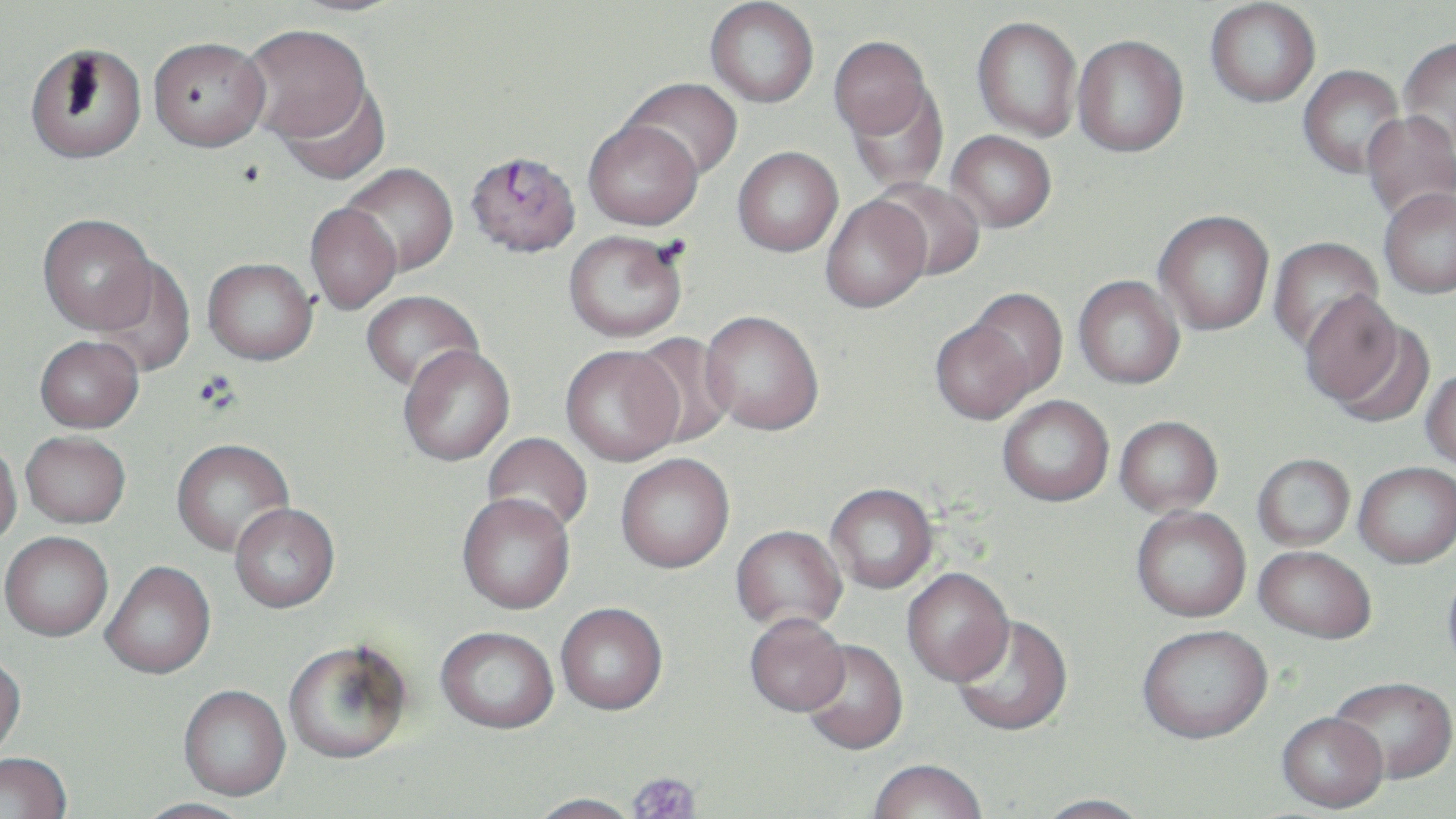
slide_level_diagnosis: Plasmodium falciparum
image_size: 1456×819 pixels
preparation: thin blood film
uninfected_red_blood_cell_locations: 'approximate bounding boxes as named x1/y1/x2/y2 corners in pixels: (x1=285, y1=0, x2=411, y2=17), (x1=705, y1=1, x2=819, y2=107), (x1=1205, y1=1, x2=1321, y2=107), (x1=972, y1=16, x2=1083, y2=141), (x1=241, y1=24, x2=373, y2=144), (x1=1072, y1=35, x2=1189, y2=157), (x1=148, y1=36, x2=270, y2=151), (x1=829, y1=36, x2=933, y2=139), (x1=1398, y1=36, x2=1456, y2=156), (x1=24, y1=42, x2=148, y2=165), (x1=1298, y1=65, x2=1405, y2=178), (x1=621, y1=77, x2=743, y2=182), (x1=275, y1=79, x2=391, y2=185), (x1=844, y1=83, x2=948, y2=191), (x1=1360, y1=111, x2=1456, y2=224), (x1=583, y1=119, x2=703, y2=230), (x1=946, y1=130, x2=1056, y2=232), (x1=733, y1=146, x2=843, y2=256), (x1=340, y1=163, x2=459, y2=276), (x1=872, y1=178, x2=986, y2=280), (x1=1379, y1=187, x2=1456, y2=298), (x1=820, y1=195, x2=930, y2=313), (x1=304, y1=203, x2=402, y2=314), (x1=1153, y1=210, x2=1274, y2=335), (x1=37, y1=213, x2=157, y2=334), (x1=563, y1=230, x2=687, y2=342), (x1=1267, y1=237, x2=1385, y2=357), (x1=92, y1=256, x2=198, y2=377), (x1=202, y1=257, x2=318, y2=364), (x1=1073, y1=275, x2=1185, y2=389), (x1=964, y1=287, x2=1068, y2=399), (x1=360, y1=290, x2=483, y2=393), (x1=1299, y1=290, x2=1407, y2=411), (x1=700, y1=310, x2=823, y2=434), (x1=930, y1=317, x2=1036, y2=425), (x1=629, y1=332, x2=738, y2=449), (x1=35, y1=335, x2=143, y2=433), (x1=398, y1=345, x2=515, y2=466), (x1=560, y1=345, x2=683, y2=465), (x1=1421, y1=368, x2=1456, y2=471), (x1=997, y1=395, x2=1114, y2=507), (x1=1114, y1=416, x2=1223, y2=517), (x1=21, y1=433, x2=130, y2=531), (x1=482, y1=433, x2=593, y2=536), (x1=171, y1=438, x2=294, y2=557), (x1=0, y1=441, x2=23, y2=550), (x1=616, y1=454, x2=735, y2=573), (x1=1252, y1=454, x2=1355, y2=551), (x1=1354, y1=462, x2=1456, y2=568), (x1=825, y1=484, x2=937, y2=594), (x1=456, y1=496, x2=575, y2=616), (x1=230, y1=505, x2=339, y2=615), (x1=1131, y1=506, x2=1251, y2=623), (x1=731, y1=526, x2=847, y2=635), (x1=0, y1=535, x2=113, y2=644), (x1=1253, y1=545, x2=1377, y2=644), (x1=101, y1=564, x2=216, y2=682), (x1=1443, y1=564, x2=1456, y2=682), (x1=901, y1=569, x2=1015, y2=688), (x1=555, y1=606, x2=668, y2=718), (x1=950, y1=616, x2=1072, y2=739), (x1=744, y1=617, x2=850, y2=719), (x1=1137, y1=626, x2=1273, y2=747), (x1=436, y1=630, x2=558, y2=737), (x1=800, y1=642, x2=908, y2=758), (x1=283, y1=643, x2=411, y2=767), (x1=0, y1=657, x2=26, y2=762), (x1=1329, y1=677, x2=1456, y2=785), (x1=178, y1=687, x2=291, y2=803), (x1=1277, y1=715, x2=1388, y2=815), (x1=1, y1=755, x2=72, y2=819), (x1=868, y1=763, x2=988, y2=819), (x1=526, y1=795, x2=641, y2=819), (x1=1033, y1=796, x2=1151, y2=819), (x1=135, y1=800, x2=253, y2=819)'
platelet_locations: 'approximate bounding boxes as named x1/y1/x2/y2 corners in pixels: (x1=626, y1=773, x2=702, y2=819)'
modality: light microscopy
field_of_view: one of a larger specimen
stain: May-Grünwald-Giemsa
plasmodium_falciparum_infected_red_blood_cell_locations: 'approximate bounding boxes as named x1/y1/x2/y2 corners in pixels: (x1=464, y1=150, x2=582, y2=257)'
magnification: 1000x